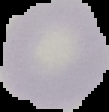

preparation = thin blood film
image type = cell region segmented out of the field of view; surrounding area masked to black
result = no Plasmodium parasites seen
image size = 109×112 pixels